Report the malaria status of this cell.
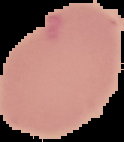
Uninfected.

image type = segmented cell region with the area outside set to black
image size = 124×142 pixels
preparation = thin blood film